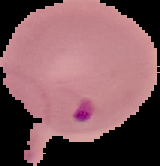

image type = cell region segmented out of the field of view; surrounding area masked to black
result = Plasmodium parasites detected
image size = 160×166 pixels
preparation = thin blood smear